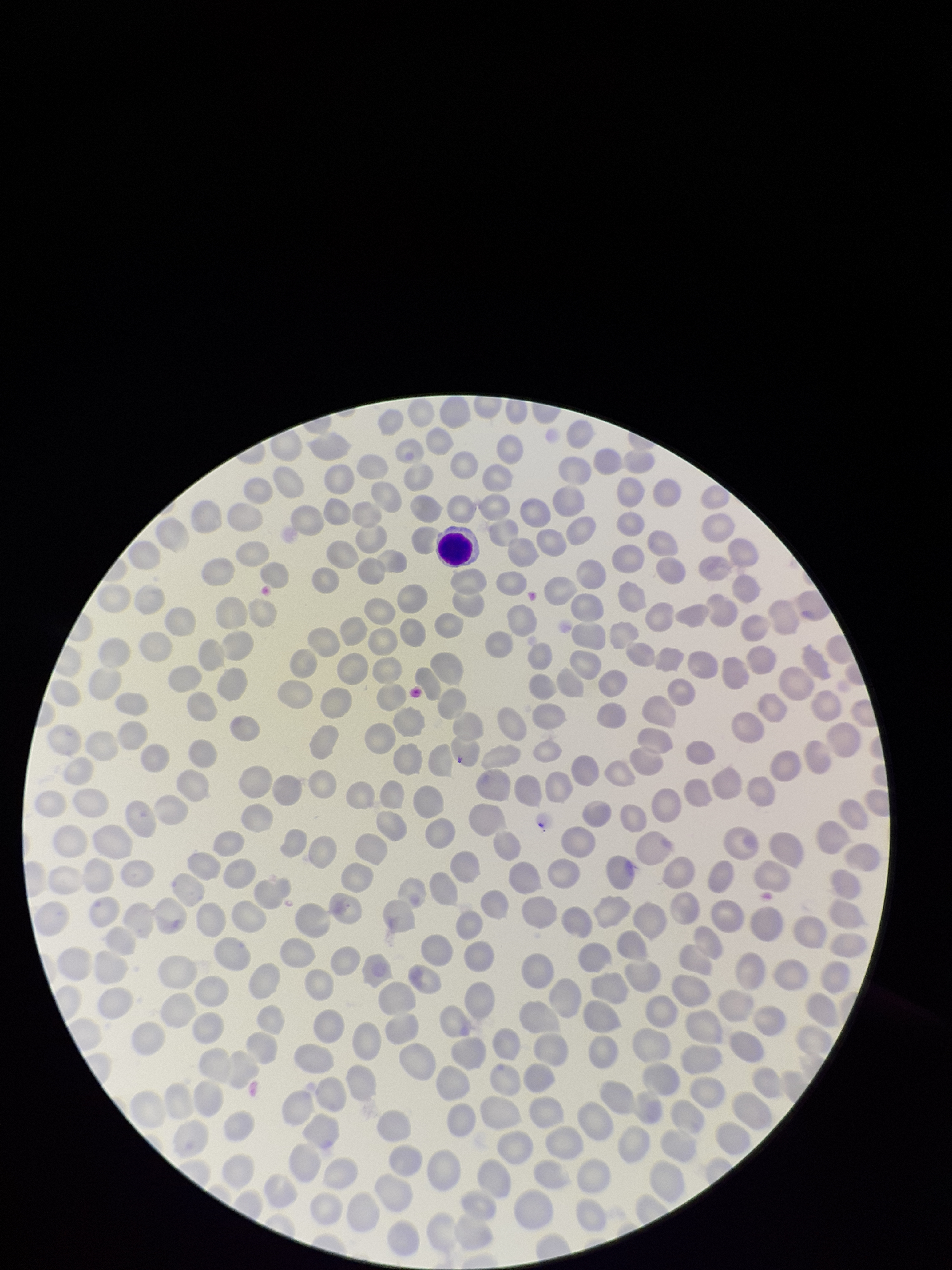
Summary:
  - Stain: Giemsa
  - Image size: 952×1270 pixels
  - Red blood cell count: 281
  - Parasitized red blood cell count: 0
  - Patient malaria status: negative
  - Preparation: thin
  - Capture: smartphone photograph through the microscope eyepiece
  - Parasitized red blood cells: none detected
  - Field of view: single